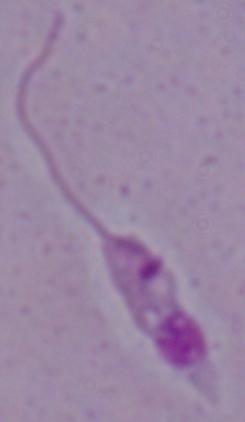
magnification: 1000x
identification: Leishmania
modality: photomicrograph